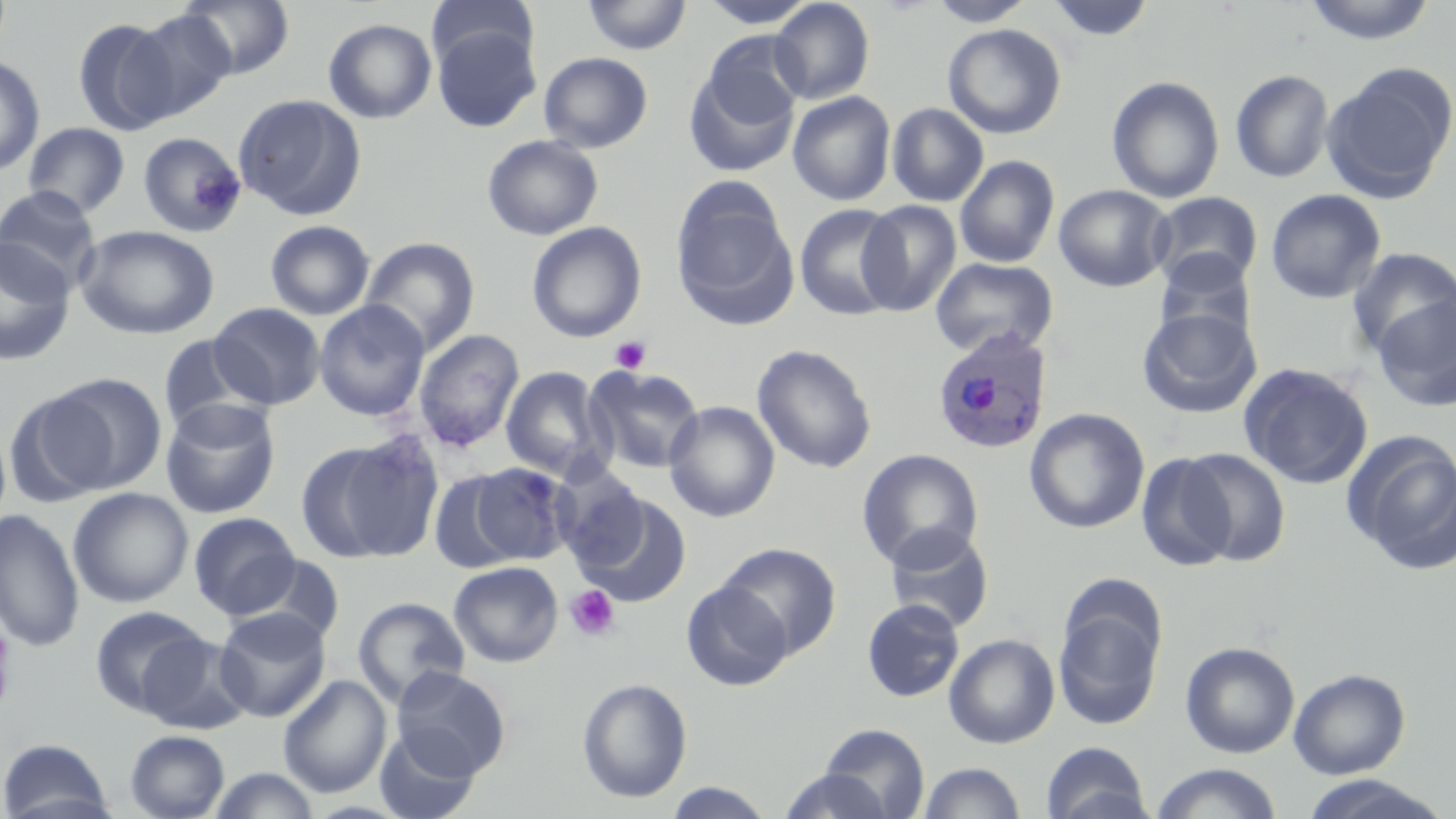
Approximate bounding boxes as (x1,y1)-(x2,y2) corner pairs in pixels. Plasmodium ovale-infected red blood cell locations: (930,326)-(1053,456). Platelet locations: (609,335)-(652,374), (565,585)-(620,642). Uninfected red blood cell locations: (179,0)-(295,79), (427,0)-(538,70), (581,0)-(692,56), (697,0)-(820,28), (928,0)-(1035,26), (1045,0)-(1157,43), (1301,0)-(1438,45), (770,1)-(875,105), (126,9)-(238,122), (72,18)-(178,135), (323,18)-(436,123), (943,23)-(1066,139), (432,25)-(541,132), (700,31)-(808,130), (539,51)-(653,153), (0,54)-(45,176), (1320,61)-(1456,203), (683,64)-(800,177), (1230,69)-(1334,183), (1106,75)-(1225,203), (787,91)-(896,205), (232,93)-(367,220), (887,103)-(988,207), (23,122)-(130,217), (137,131)-(246,238), (481,134)-(603,241), (954,155)-(1060,268), (672,183)-(797,329), (1053,184)-(1174,292), (0,185)-(101,291), (1265,188)-(1386,304), (1148,192)-(1264,291), (857,200)-(962,316), (794,203)-(904,321), (264,219)-(376,321), (527,221)-(646,343), (75,225)-(219,339), (360,237)-(480,355), (0,238)-(75,365), (1347,247)-(1456,359), (1154,250)-(1257,343), (930,257)-(1058,359), (1372,294)-(1456,412), (314,299)-(430,421), (209,302)-(325,409), (1137,306)-(1262,418), (413,329)-(525,452), (157,333)-(269,436), (752,344)-(876,473), (1238,362)-(1374,489), (500,366)-(609,479), (584,366)-(705,474), (42,373)-(169,494), (5,388)-(116,507), (159,398)-(281,519), (663,401)-(780,522), (1024,408)-(1149,534), (1344,431)-(1456,573), (300,438)-(440,564), (1179,447)-(1292,566), (856,449)-(983,570), (1135,452)-(1237,572), (469,461)-(576,565), (428,472)-(520,572), (68,487)-(193,608), (573,491)-(692,608), (0,508)-(85,652), (188,512)-(301,619), (883,524)-(994,633), (716,542)-(841,658), (240,554)-(346,647), (448,560)-(563,668), (681,580)-(793,691), (1052,594)-(1165,731), (353,596)-(470,706), (861,598)-(965,702), (89,605)-(209,715), (213,607)-(331,722), (137,631)-(253,735), (944,633)-(1060,749), (1180,641)-(1300,758), (391,666)-(511,778), (1288,668)-(1410,779), (278,676)-(391,797), (576,677)-(692,804), (817,723)-(929,818), (372,729)-(481,819), (124,730)-(230,819), (0,738)-(115,819), (1041,741)-(1152,819), (917,761)-(1027,818), (1150,763)-(1283,819), (207,767)-(322,819), (776,768)-(898,819), (1299,774)-(1450,818), (661,781)-(778,818). Slide-level diagnosis: Plasmodium ovale. Image is 1456×819 pixels. Captured at 1000x magnification. May-Grünwald-Giemsa-stained preparation. Optical microscopy. One field of a larger specimen. Thin blood film.